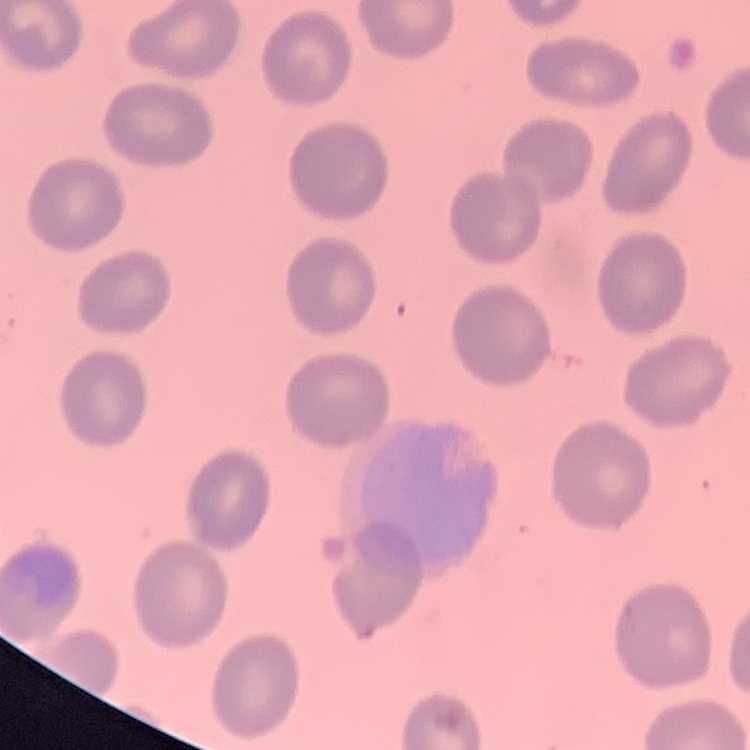

{
  "erythrocyte_morphology": "no rouleaux formation",
  "stain": "Field's or Giemsa",
  "preparation": "thin blood film",
  "image_type": "square crop of a larger photomicrograph"
}